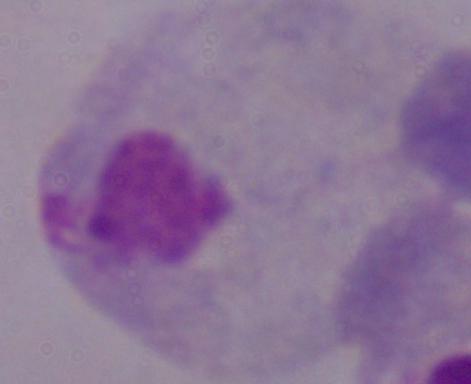
modality = micrograph
identification = trichomonad
magnification = 1000x